Comment on the morphology of the red blood cells.
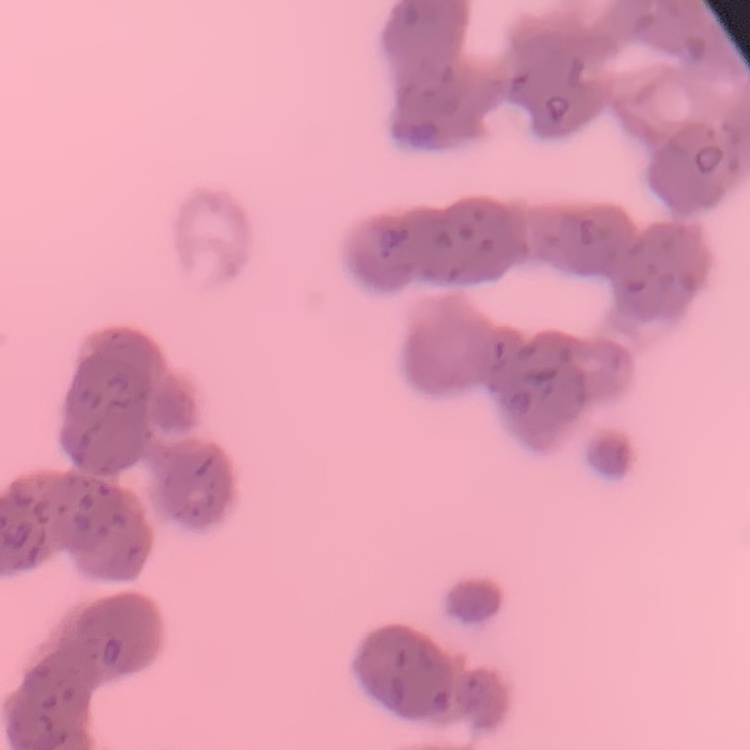

They show rouleaux formation.

Thin blood film. Square crop of a larger photomicrograph. Field's or Giemsa stain.